Assess the morphology of the red blood cells.
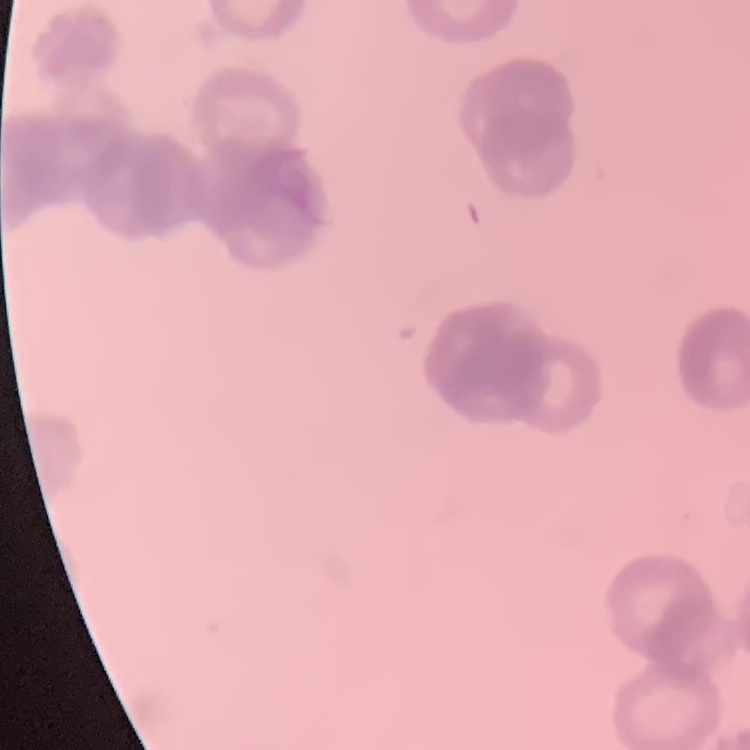

They show rouleaux formation.

preparation = thin peripheral smear
image type = one tile cut from a larger photomicrograph
stain = Field's or Giemsa